Name the parasite shown.
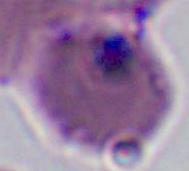

Plasmodium.

400x or 1000x magnification. Photomicrograph.